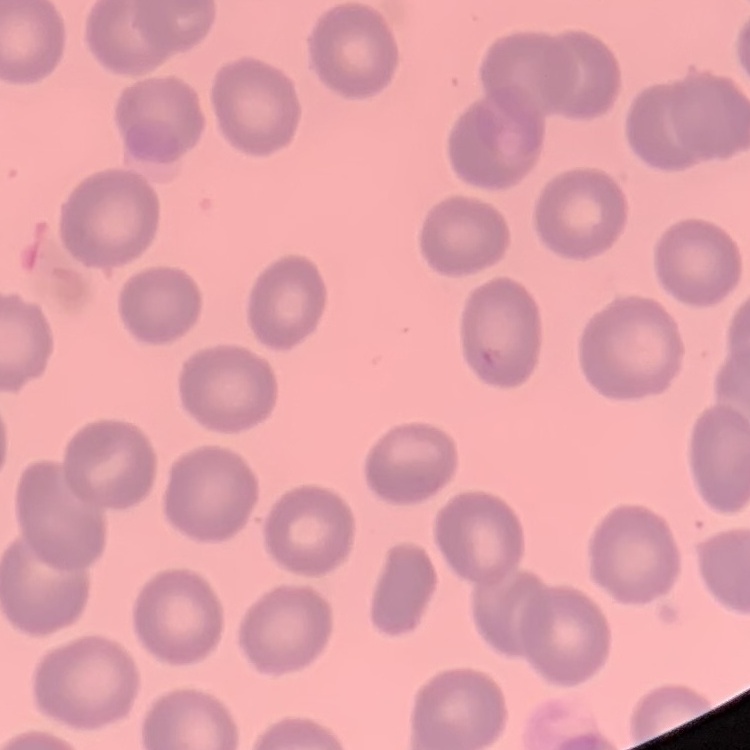

{
  "erythrocyte_morphology": "no rouleaux formation",
  "preparation": "thin blood film",
  "stain": "Field's or Giemsa",
  "image_type": "one tile cut from a larger photomicrograph"
}